Give the position of every Plasmodium parasite visible.
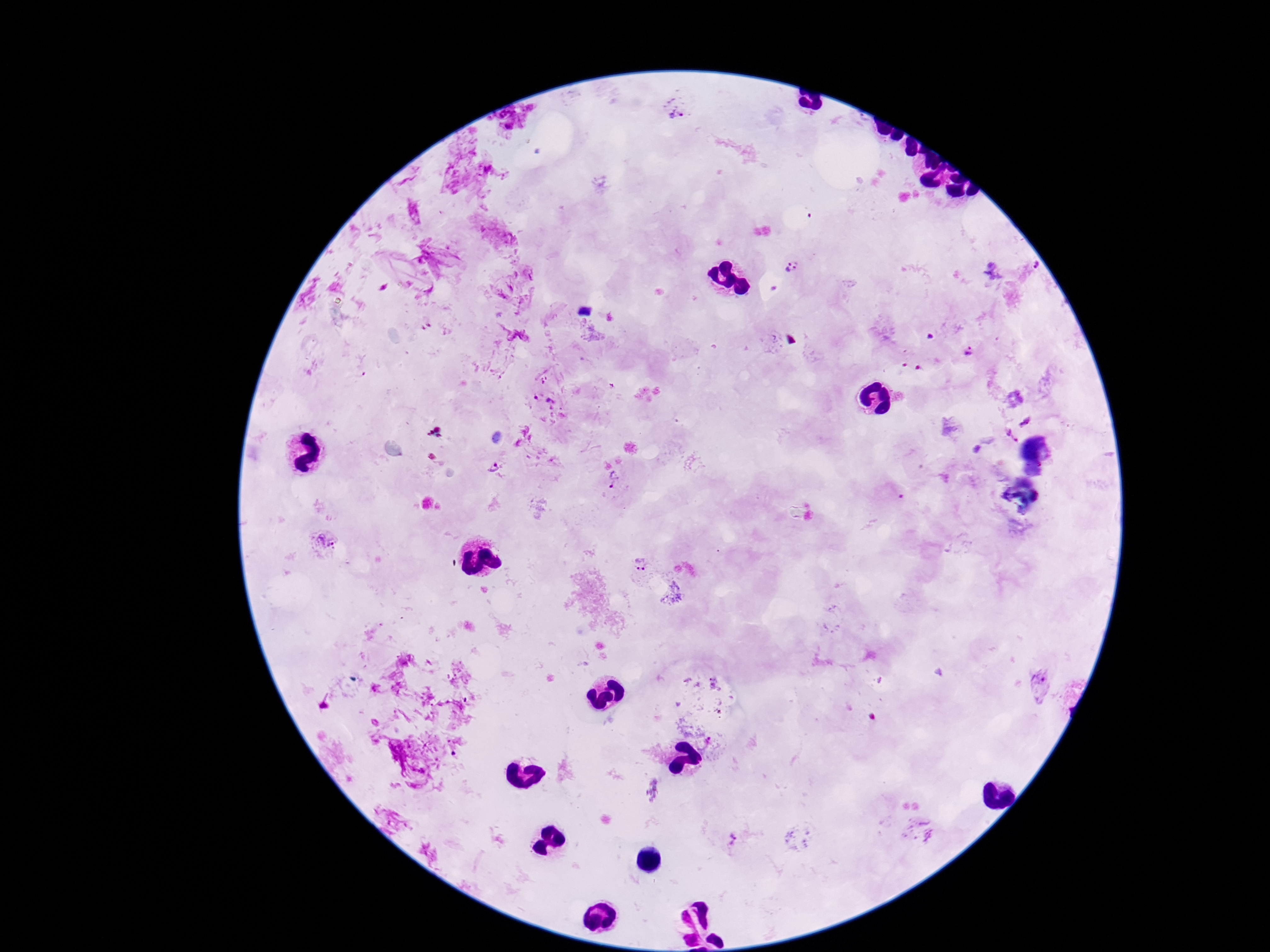

Approximate centers as (x, y) in pixels.
Plasmodium parasites: (676, 107), (1039, 264), (792, 267), (971, 352), (543, 395), (1025, 420), (1011, 435), (494, 467), (614, 481), (325, 542), (638, 568), (731, 839).

Thick blood film. Image is 1270×952 pixels. One field from this slide. Giemsa-stained preparation. Smartphone photograph taken through the microscope eyepiece. Patient malaria status: positive. 100x magnification.